Name the cell type shown.
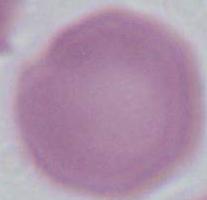

An erythrocyte.

Summary:
  - Magnification: 1000x
  - Modality: micrograph